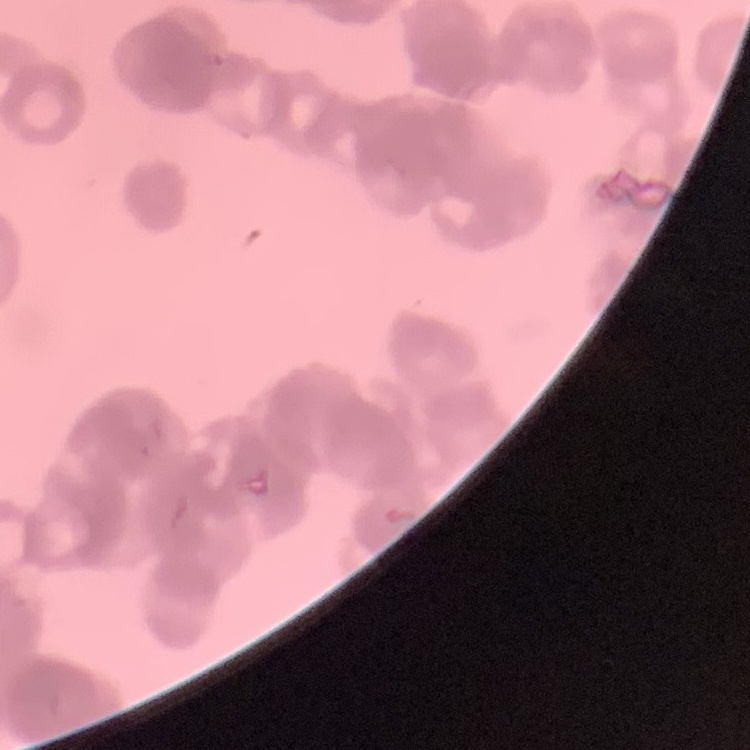 The erythrocytes show rouleaux formation. Field's or Giemsa stain. Square crop of a larger photomicrograph. Thin blood film.